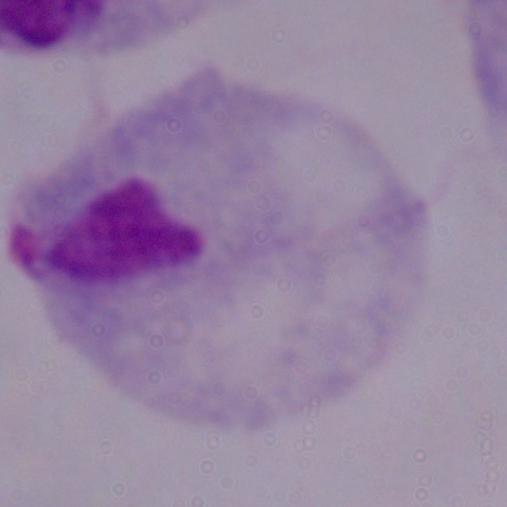
magnification: 1000x
modality: micrograph
identification: trichomonad